Assess this cell for malaria.
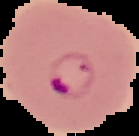

Parasitized.

image size = 139×136 pixels
preparation = thin blood smear
image type = segmented cell region with the area outside set to black